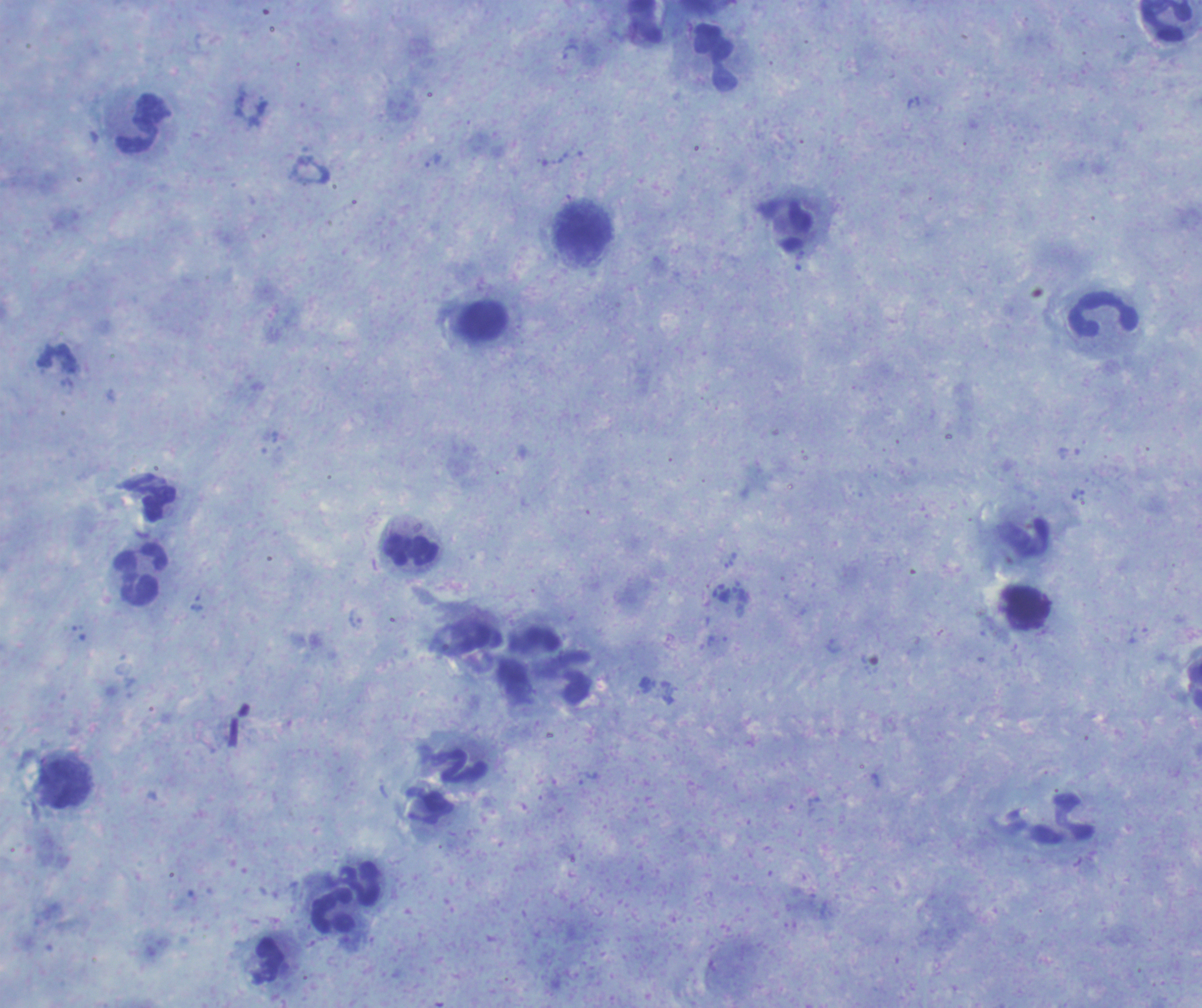

coordinate format = approximate centers as {x, y} in pixels
leukocyte locations = {1166, 21}, {715, 57}, {143, 124}, {584, 233}, {1105, 316}, {411, 550}, {140, 576}, {1028, 609}, {460, 768}, {67, 786}, {334, 912}
result = no Plasmodium parasites seen
background quality = good
coloration quality = good
preparation = thick blood film
magnification = 100x
image size = 1202×1008 pixels
stain = Romanowsky
context = previously used in an actual diagnosis
field of view = one from this slide